Assess the morphology of the red blood cells.
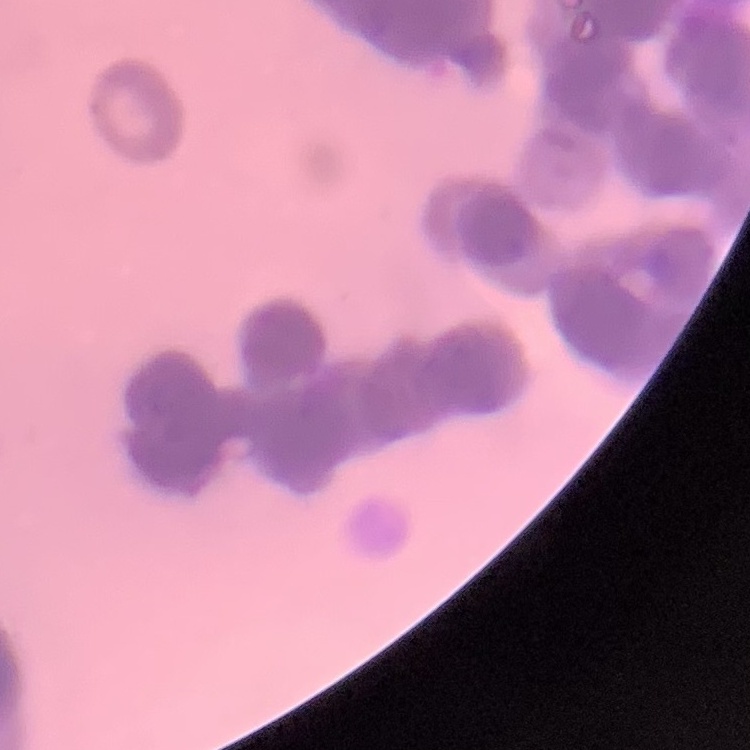

Rouleaux formation.

Summary:
  - Stain: Field's or Giemsa
  - Preparation: thin blood film
  - Image type: square crop of a larger photomicrograph